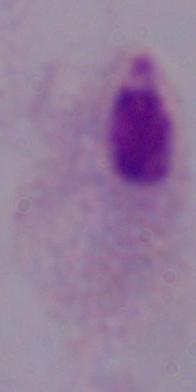 A trichomonad is seen. 1000x magnification. Photomicrograph.